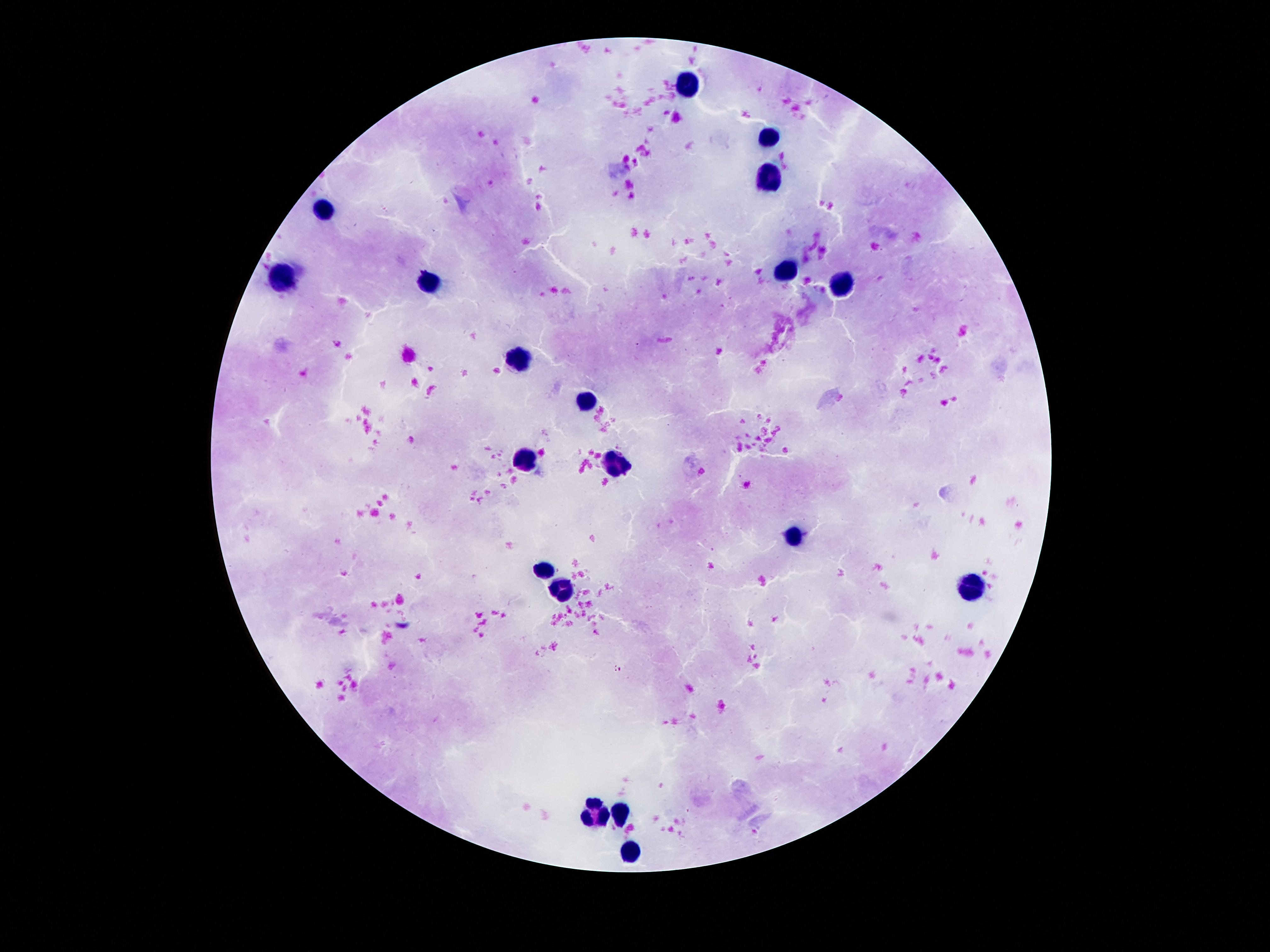
patient malaria status = negative
magnification = 100x
field of view = one from this slide
image size = 1270×952 pixels
capture = smartphone camera through the microscope eyepiece
stain = Giemsa
preparation = thick blood film
leukocyte locations = approximate object centers, in pixels from the top-left corner: (x=688, y=83), (x=770, y=135), (x=767, y=170), (x=326, y=211), (x=786, y=274), (x=282, y=281), (x=429, y=282), (x=844, y=291), (x=515, y=356), (x=585, y=403), (x=527, y=459), (x=613, y=465), (x=793, y=536), (x=543, y=573), (x=968, y=583), (x=564, y=586), (x=595, y=810), (x=620, y=814), (x=632, y=852)